Locate platelets.
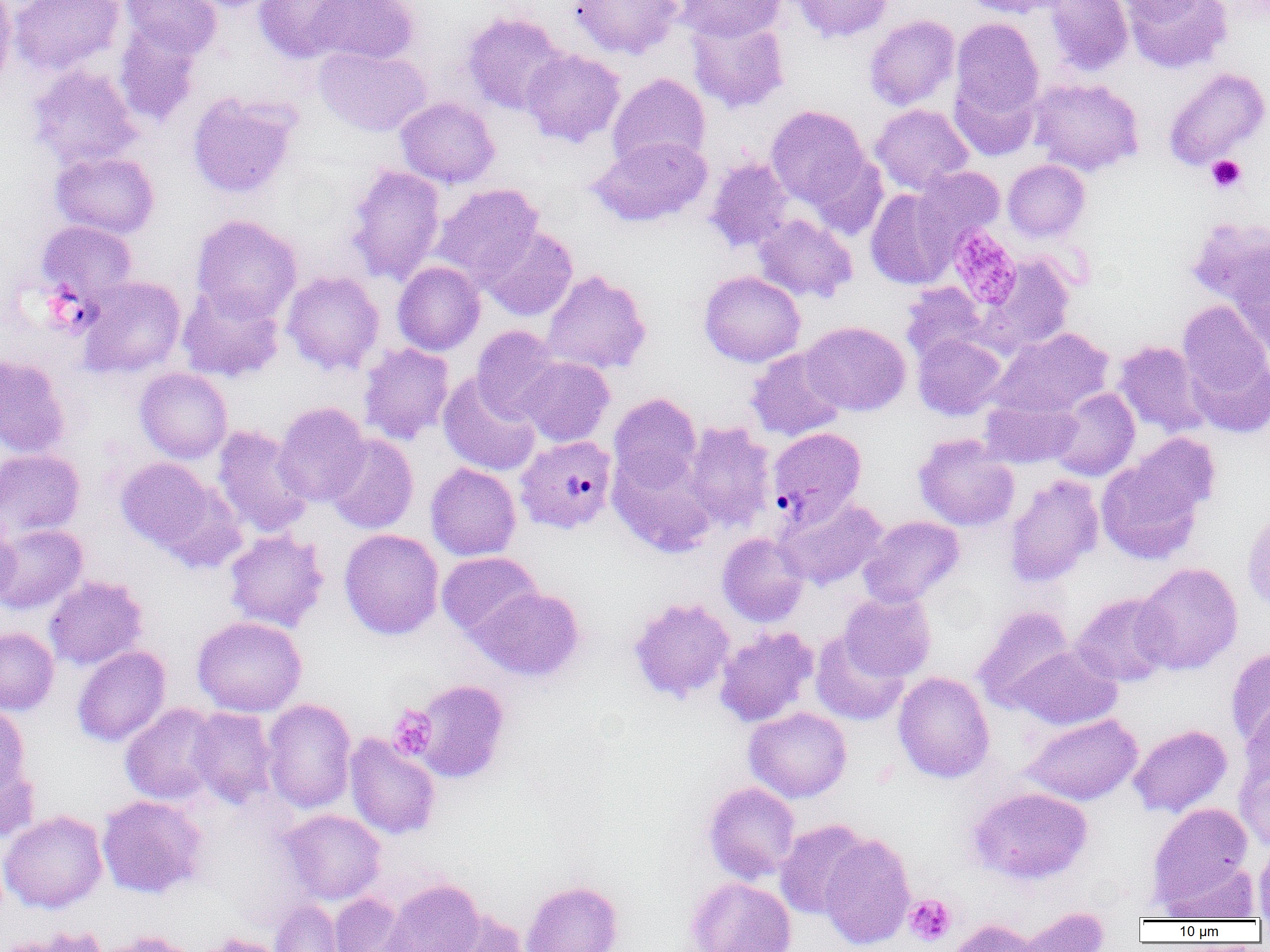

Approximate bounding boxes as named x1/y1/x2/y2 corners in pixels.
Platelets: (x1=1206, y1=154, x2=1246, y2=193), (x1=948, y1=226, x2=1022, y2=309), (x1=388, y1=706, x2=437, y2=761), (x1=904, y1=894, x2=956, y2=946).

Uninfected red blood cell locations: (x1=0, y1=0, x2=16, y2=92), (x1=7, y1=0, x2=125, y2=76), (x1=121, y1=0, x2=221, y2=59), (x1=181, y1=0, x2=282, y2=12), (x1=254, y1=0, x2=362, y2=63), (x1=307, y1=0, x2=421, y2=64), (x1=569, y1=0, x2=683, y2=59), (x1=677, y1=0, x2=785, y2=42), (x1=789, y1=0, x2=894, y2=43), (x1=960, y1=0, x2=1067, y2=18), (x1=1045, y1=0, x2=1133, y2=76), (x1=1112, y1=0, x2=1209, y2=23), (x1=1124, y1=0, x2=1232, y2=73), (x1=462, y1=12, x2=567, y2=115), (x1=864, y1=15, x2=960, y2=111), (x1=686, y1=16, x2=790, y2=114), (x1=951, y1=18, x2=1044, y2=120), (x1=114, y1=23, x2=202, y2=128), (x1=314, y1=46, x2=432, y2=137), (x1=520, y1=49, x2=626, y2=147), (x1=27, y1=65, x2=141, y2=169), (x1=1162, y1=67, x2=1269, y2=171), (x1=608, y1=72, x2=711, y2=173), (x1=950, y1=74, x2=1041, y2=160), (x1=1028, y1=77, x2=1144, y2=176), (x1=186, y1=91, x2=301, y2=199), (x1=395, y1=97, x2=500, y2=188), (x1=870, y1=104, x2=974, y2=196), (x1=766, y1=105, x2=870, y2=208), (x1=588, y1=136, x2=712, y2=227), (x1=50, y1=150, x2=160, y2=239), (x1=808, y1=153, x2=888, y2=240), (x1=705, y1=157, x2=793, y2=253), (x1=1003, y1=159, x2=1090, y2=242), (x1=345, y1=164, x2=445, y2=286), (x1=915, y1=166, x2=1005, y2=246), (x1=431, y1=183, x2=544, y2=286), (x1=866, y1=189, x2=957, y2=289), (x1=753, y1=214, x2=857, y2=303), (x1=191, y1=215, x2=302, y2=323), (x1=1184, y1=216, x2=1269, y2=309), (x1=36, y1=220, x2=138, y2=302), (x1=479, y1=226, x2=579, y2=321), (x1=1230, y1=253, x2=1270, y2=358), (x1=974, y1=255, x2=1075, y2=357), (x1=392, y1=261, x2=485, y2=355), (x1=541, y1=269, x2=652, y2=376), (x1=699, y1=270, x2=806, y2=367), (x1=282, y1=271, x2=384, y2=375), (x1=78, y1=276, x2=186, y2=379), (x1=900, y1=283, x2=987, y2=364), (x1=177, y1=286, x2=284, y2=383), (x1=1177, y1=300, x2=1270, y2=410), (x1=800, y1=321, x2=911, y2=416), (x1=471, y1=325, x2=564, y2=422), (x1=991, y1=327, x2=1114, y2=419), (x1=912, y1=333, x2=1006, y2=420), (x1=1113, y1=341, x2=1210, y2=438), (x1=358, y1=342, x2=455, y2=445), (x1=1185, y1=345, x2=1270, y2=440), (x1=746, y1=347, x2=848, y2=442), (x1=0, y1=355, x2=71, y2=458), (x1=516, y1=356, x2=614, y2=446), (x1=134, y1=368, x2=232, y2=463), (x1=439, y1=373, x2=541, y2=476), (x1=1048, y1=387, x2=1140, y2=481), (x1=608, y1=392, x2=702, y2=490), (x1=979, y1=397, x2=1081, y2=468), (x1=273, y1=402, x2=371, y2=507), (x1=683, y1=421, x2=777, y2=530), (x1=213, y1=426, x2=314, y2=538), (x1=324, y1=433, x2=419, y2=534), (x1=913, y1=433, x2=1019, y2=531), (x1=1125, y1=433, x2=1220, y2=521), (x1=0, y1=449, x2=85, y2=539), (x1=607, y1=450, x2=718, y2=558), (x1=1096, y1=450, x2=1210, y2=565), (x1=116, y1=457, x2=220, y2=554), (x1=425, y1=463, x2=521, y2=561), (x1=1004, y1=474, x2=1104, y2=588), (x1=775, y1=496, x2=888, y2=590), (x1=1242, y1=509, x2=1270, y2=613), (x1=858, y1=515, x2=965, y2=607), (x1=0, y1=516, x2=21, y2=609), (x1=0, y1=524, x2=87, y2=614), (x1=339, y1=528, x2=444, y2=640), (x1=224, y1=530, x2=329, y2=632), (x1=717, y1=532, x2=810, y2=627), (x1=437, y1=551, x2=543, y2=639), (x1=1135, y1=562, x2=1243, y2=675), (x1=43, y1=576, x2=148, y2=669), (x1=470, y1=586, x2=585, y2=681), (x1=839, y1=591, x2=936, y2=681), (x1=1071, y1=592, x2=1176, y2=686), (x1=628, y1=597, x2=736, y2=703), (x1=972, y1=605, x2=1076, y2=711), (x1=192, y1=616, x2=307, y2=716), (x1=715, y1=626, x2=819, y2=727), (x1=0, y1=627, x2=59, y2=715), (x1=810, y1=631, x2=909, y2=726), (x1=1008, y1=644, x2=1122, y2=729), (x1=72, y1=645, x2=171, y2=747), (x1=1225, y1=646, x2=1270, y2=750), (x1=893, y1=671, x2=994, y2=783), (x1=410, y1=679, x2=511, y2=784), (x1=1239, y1=697, x2=1270, y2=790), (x1=261, y1=698, x2=357, y2=814), (x1=0, y1=702, x2=31, y2=798), (x1=120, y1=703, x2=222, y2=805), (x1=187, y1=707, x2=277, y2=807), (x1=744, y1=707, x2=852, y2=802), (x1=1022, y1=713, x2=1142, y2=805), (x1=1129, y1=724, x2=1233, y2=818), (x1=344, y1=734, x2=441, y2=839), (x1=0, y1=757, x2=40, y2=845), (x1=1235, y1=757, x2=1270, y2=853), (x1=703, y1=782, x2=800, y2=883), (x1=967, y1=786, x2=1092, y2=885), (x1=97, y1=795, x2=207, y2=899), (x1=1147, y1=802, x2=1253, y2=908), (x1=280, y1=809, x2=386, y2=904), (x1=0, y1=810, x2=109, y2=914), (x1=774, y1=819, x2=871, y2=920), (x1=819, y1=833, x2=915, y2=950), (x1=1253, y1=843, x2=1270, y2=919), (x1=1160, y1=860, x2=1261, y2=921), (x1=686, y1=876, x2=797, y2=952), (x1=383, y1=879, x2=485, y2=952), (x1=521, y1=880, x2=624, y2=952), (x1=328, y1=892, x2=412, y2=952), (x1=269, y1=900, x2=345, y2=952), (x1=1016, y1=906, x2=1111, y2=951), (x1=437, y1=909, x2=531, y2=952), (x1=947, y1=918, x2=1042, y2=952), (x1=5, y1=926, x2=109, y2=952), (x1=93, y1=930, x2=201, y2=952), (x1=195, y1=933, x2=290, y2=952). Plasmodium vivax-infected red blood cell locations: (x1=767, y1=427, x2=867, y2=525), (x1=515, y1=435, x2=617, y2=534). Slide-level diagnosis: Plasmodium vivax. 1000x magnification. Light microscopy. Image is 1270×952 pixels. One field of a larger specimen. Thin blood film.